Assess this cell for malaria.
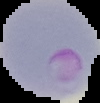
Parasitized.

Summary:
  - Image type: cell region segmented out of the field of view; surrounding area masked to black
  - Image size: 100×103 pixels
  - Preparation: thin blood film